Locate every malaria parasite.
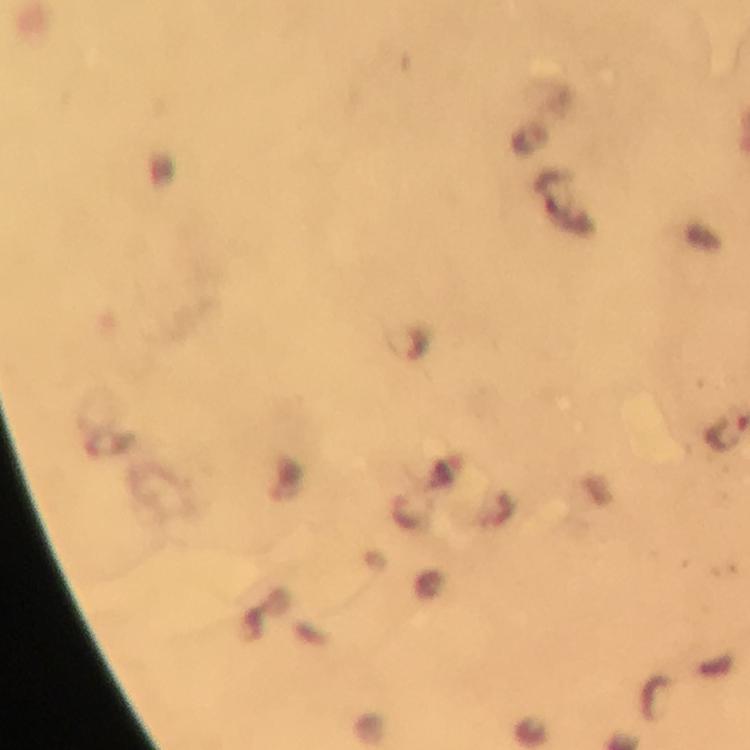

Approximate centers as [x, y] in pixels.
Malaria parasites: [407, 345], [407, 509].

Summary:
  - Immersion oil: applied
  - Magnification: 100x
  - Image size: 750×750 pixels
  - Preparation: thick smear
  - Capture: smartphone photograph through a microscope
  - Context: from a malaria diagnostic workup
  - Cropped from: one field of view
  - Stain: Giemsa